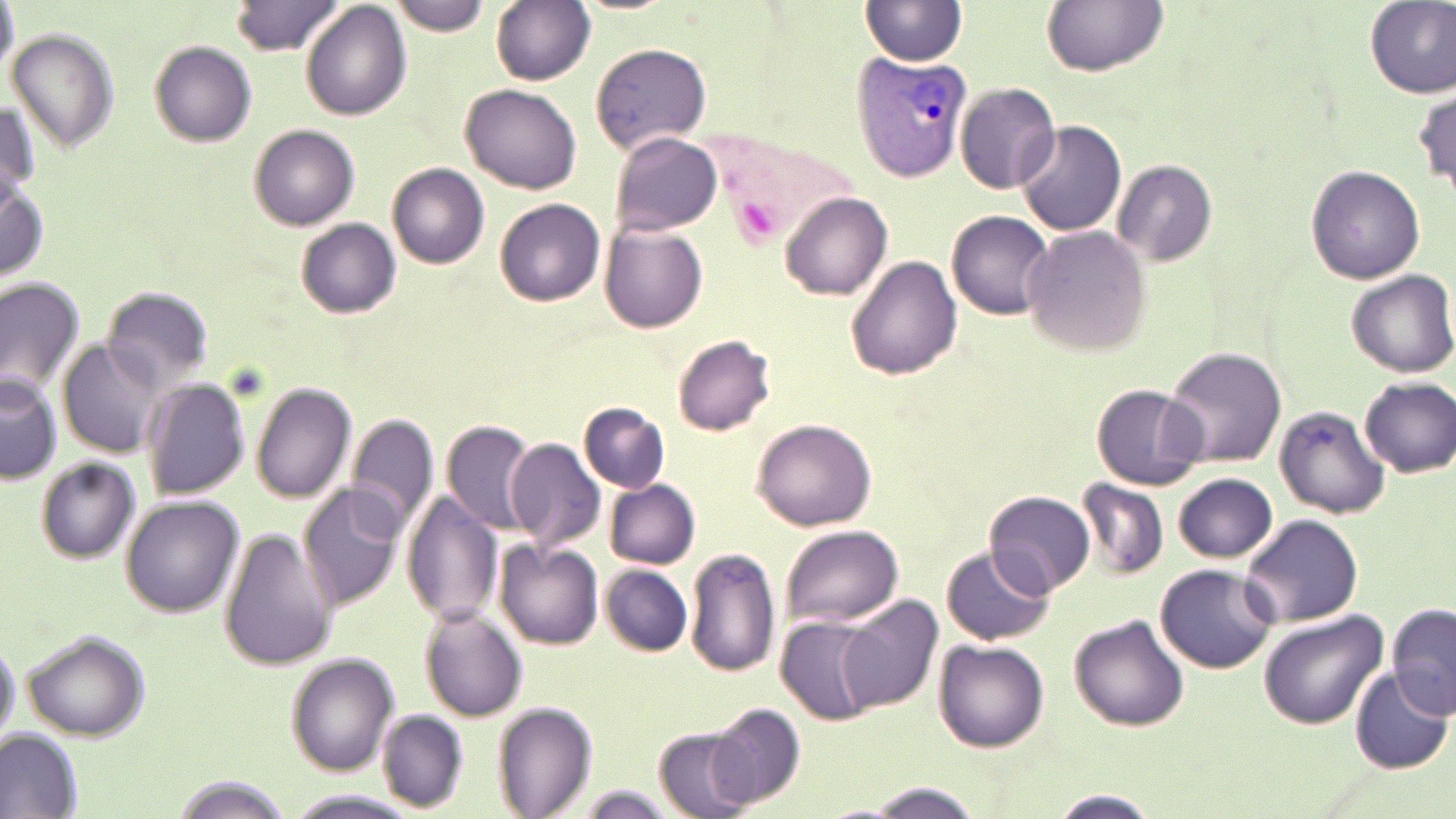 Approximate bounding boxes as (x1, y1, x2, y2) in pixels. Uninfected red blood cell locations: (232, 0, 344, 57), (490, 0, 595, 86), (1041, 0, 1169, 74), (0, 1, 18, 84), (301, 1, 410, 120), (390, 1, 492, 34), (863, 1, 968, 66), (1363, 1, 1455, 98), (8, 29, 119, 152), (589, 41, 713, 155), (150, 42, 257, 145), (954, 82, 1061, 193), (461, 83, 582, 194), (1413, 89, 1456, 190), (2, 101, 41, 199), (1015, 120, 1126, 238), (250, 124, 359, 231), (608, 131, 722, 237), (1112, 159, 1216, 267), (388, 162, 491, 270), (1305, 165, 1425, 285), (1, 176, 49, 283), (781, 192, 893, 300), (495, 198, 606, 307), (947, 211, 1055, 319), (295, 218, 400, 318), (600, 223, 707, 333), (1020, 225, 1150, 355), (846, 255, 962, 379), (1345, 271, 1456, 377), (0, 277, 84, 401), (100, 285, 213, 394), (674, 334, 777, 435), (59, 339, 167, 455), (1162, 346, 1287, 468), (2, 377, 61, 484), (142, 377, 251, 500), (1359, 377, 1456, 476), (251, 381, 357, 503), (1091, 382, 1209, 489), (579, 401, 671, 492), (1275, 405, 1390, 519), (345, 412, 440, 535), (752, 418, 876, 531), (440, 419, 534, 534), (425, 434, 524, 598), (505, 440, 607, 558), (36, 457, 141, 563), (1173, 473, 1278, 563), (605, 479, 700, 568), (1075, 479, 1170, 581), (297, 483, 407, 609), (983, 490, 1096, 600), (402, 491, 504, 627), (122, 497, 244, 617), (1241, 514, 1364, 628), (778, 523, 902, 629), (218, 530, 339, 671), (497, 541, 604, 649), (940, 543, 1057, 648), (684, 547, 783, 678), (1155, 563, 1281, 672), (600, 565, 694, 655), (834, 594, 941, 712), (1388, 602, 1456, 718), (420, 607, 527, 721), (1257, 611, 1389, 728), (776, 615, 878, 726), (1070, 616, 1188, 730), (0, 628, 20, 750), (22, 631, 150, 742), (934, 640, 1048, 751), (286, 652, 400, 774), (1350, 668, 1453, 774), (492, 701, 597, 819), (703, 702, 807, 810), (377, 710, 467, 809), (0, 726, 84, 819), (653, 726, 755, 818), (167, 774, 293, 818), (856, 782, 988, 817), (563, 784, 684, 818), (286, 789, 423, 819), (1047, 791, 1163, 819). Plasmodium vivax-infected red blood cell locations: (851, 49, 971, 185), (705, 126, 859, 256). Slide-level diagnosis: Plasmodium vivax. Image is 1456×819 pixels. May-Grünwald-Giemsa stain. Captured at 1000x magnification. Single field of view. Optical microscopy. Thin blood smear.